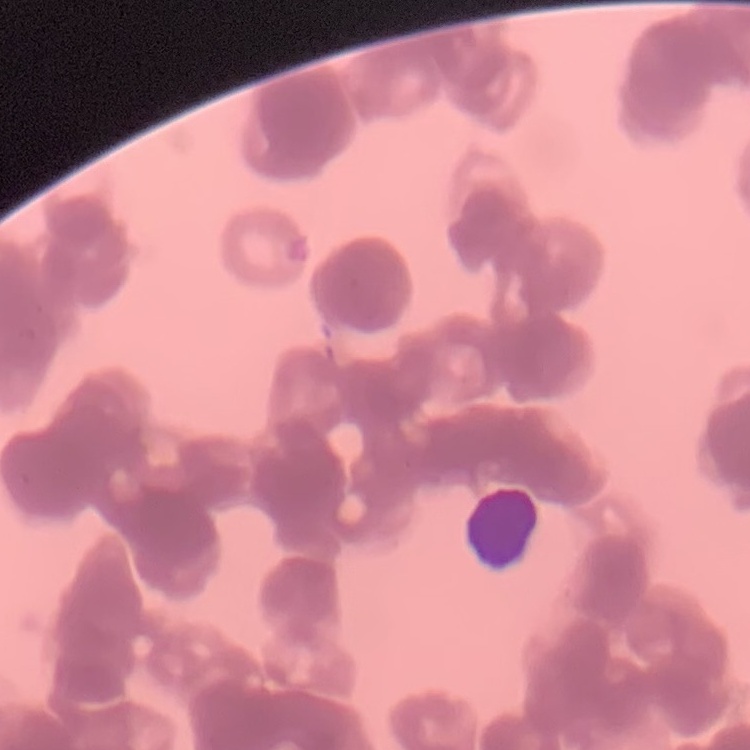
Summary:
  - Erythrocyte morphology: rouleaux formation
  - Preparation: thin peripheral smear
  - Image type: square crop of a larger photomicrograph
  - Stain: Field's or Giemsa